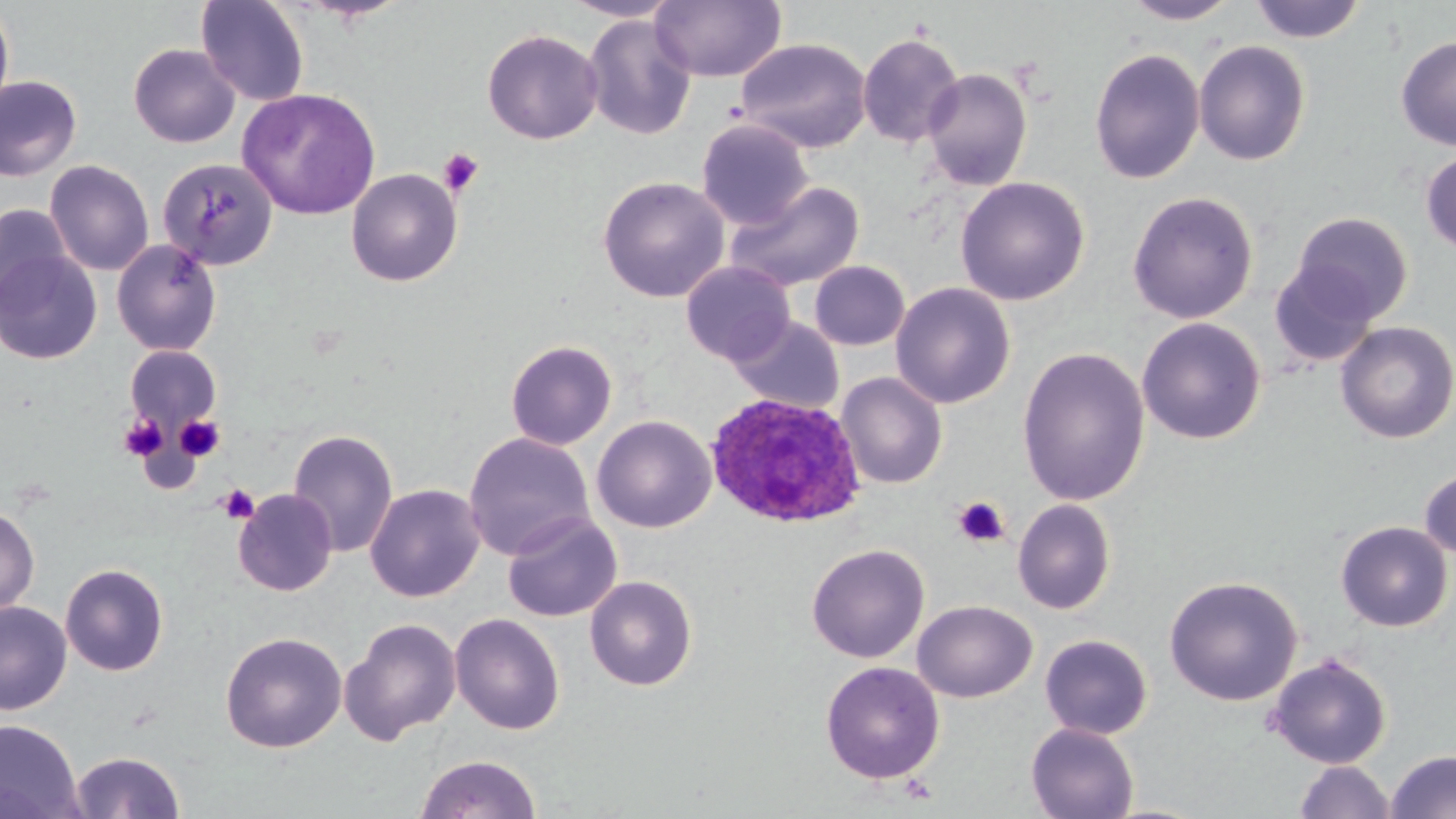
Approximate bounding boxes as [x1, y1, x2, y2] in pixels. Plasmodium ovale-infected red blood cell locations: [704, 392, 866, 529]. Platelet locations: [438, 147, 484, 197], [119, 413, 167, 462], [175, 415, 225, 462], [217, 484, 260, 525], [953, 496, 1010, 548]. Uninfected red blood cell locations: [196, 0, 310, 107], [559, 0, 682, 22], [651, 0, 786, 84], [1121, 0, 1241, 25], [1249, 0, 1366, 43], [0, 1, 15, 125], [583, 14, 697, 140], [482, 28, 603, 145], [858, 31, 965, 148], [1395, 35, 1456, 151], [735, 38, 872, 154], [1193, 40, 1311, 166], [128, 43, 241, 148], [1089, 48, 1205, 184], [921, 68, 1032, 191], [0, 75, 82, 182], [237, 87, 381, 219], [696, 118, 813, 230], [1420, 150, 1456, 255], [157, 158, 279, 270], [44, 160, 154, 276], [346, 168, 463, 287], [597, 176, 730, 303], [955, 176, 1090, 306], [726, 180, 865, 292], [1126, 190, 1258, 324], [0, 204, 72, 316], [1290, 212, 1414, 325], [111, 239, 222, 356], [0, 248, 102, 365], [681, 261, 796, 366], [809, 261, 910, 350], [1269, 261, 1380, 368], [891, 282, 1016, 409], [729, 316, 844, 415], [1136, 317, 1266, 445], [1335, 321, 1455, 444], [505, 339, 618, 450], [125, 346, 221, 431], [1016, 346, 1150, 507], [836, 372, 947, 489], [592, 415, 716, 533], [287, 428, 399, 558], [463, 432, 594, 560], [1419, 466, 1456, 560], [365, 484, 485, 602], [233, 489, 338, 596], [1013, 499, 1116, 614], [0, 504, 39, 619], [502, 511, 622, 622], [1336, 521, 1453, 631], [806, 543, 930, 663], [60, 563, 169, 676], [584, 575, 698, 691], [1164, 575, 1303, 706], [912, 600, 1037, 703], [0, 601, 72, 715], [449, 613, 565, 735], [340, 617, 462, 746], [220, 631, 347, 753], [1039, 634, 1153, 740], [1266, 653, 1392, 769], [820, 661, 945, 784], [0, 718, 84, 819], [1026, 723, 1139, 819], [70, 750, 185, 818], [1386, 750, 1456, 819], [414, 753, 542, 818], [1294, 760, 1395, 818]. Slide-level diagnosis: Plasmodium ovale. Optical microscopy. One field of a larger specimen. May-Grünwald-Giemsa stain. Captured at 1000x magnification. Thin blood film. Image is 1456×819 pixels.